Name the cell type shown.
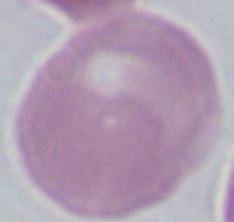

This is an erythrocyte.

1000x magnification. Micrograph.